State which parasite is depicted.
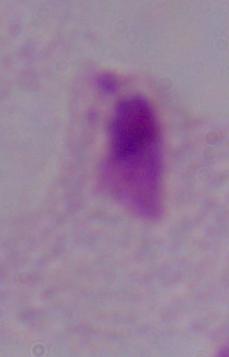

A trichomonad.

Summary:
  - Modality: photomicrograph
  - Magnification: 1000x